Locate every Plasmodium falciparum-infected red blood cell.
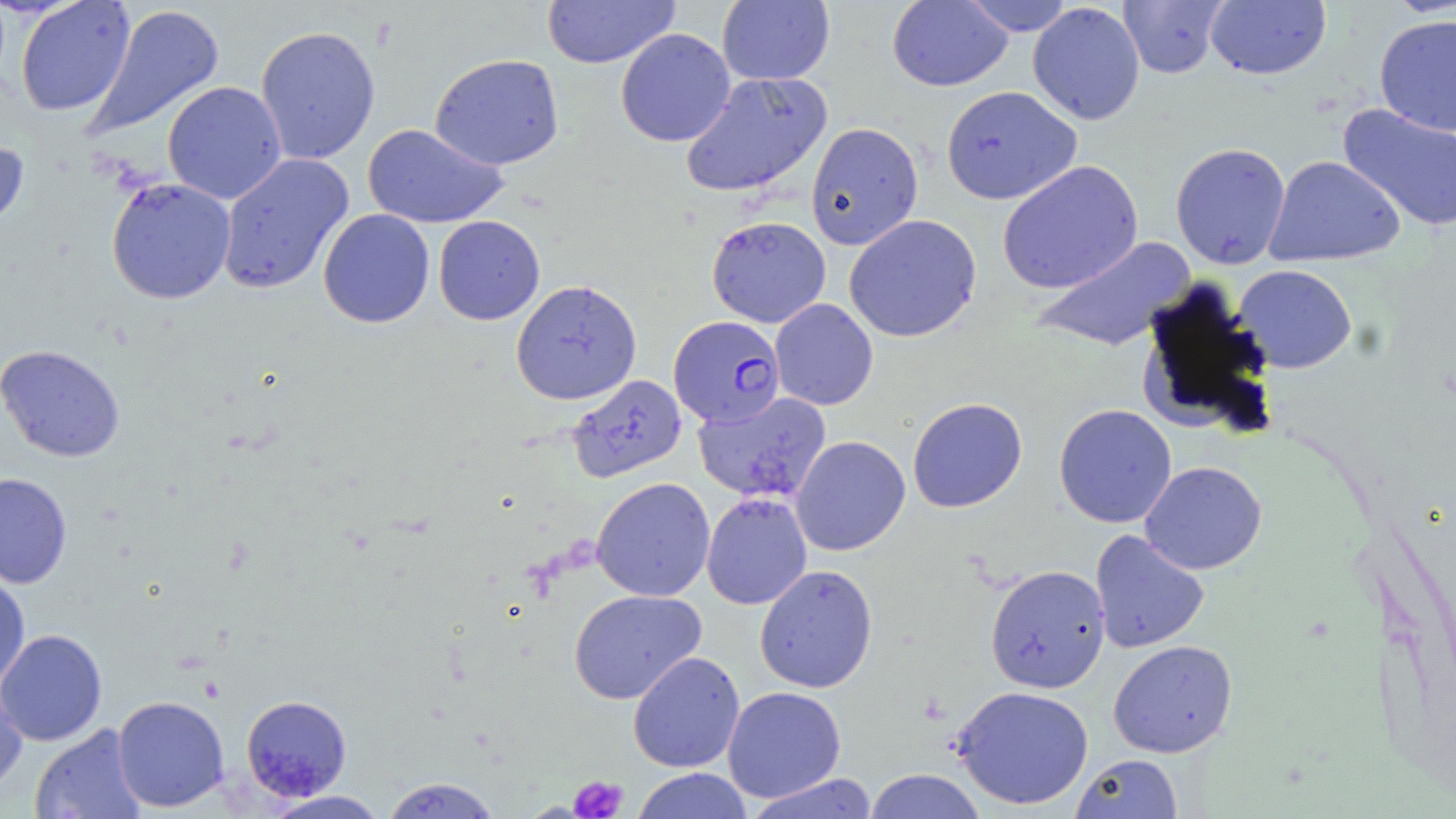
Approximate bounding boxes as (x1,y1)-(x2,y2) corner pairs in pixels.
Plasmodium falciparum-infected red blood cells: (668,315)-(786,427).

Uninfected red blood cell locations: (542,0)-(680,69), (887,0)-(1013,91), (960,0)-(1076,36), (1117,0)-(1228,79), (1205,0)-(1331,80), (15,1)-(136,117), (717,1)-(835,85), (1027,2)-(1145,126), (84,4)-(225,139), (1374,14)-(1456,137), (255,24)-(381,165), (615,28)-(736,147), (429,53)-(564,170), (679,70)-(833,198), (162,81)-(287,204), (941,85)-(1082,205), (1337,103)-(1456,233), (805,121)-(924,251), (362,123)-(508,229), (0,136)-(29,240), (1170,142)-(1291,269), (216,153)-(354,295), (1264,155)-(1406,267), (997,160)-(1143,294), (106,177)-(236,304), (318,209)-(435,328), (844,214)-(982,343), (433,215)-(545,325), (706,215)-(831,328), (1030,235)-(1197,352), (1232,264)-(1357,374), (1137,278)-(1278,440), (511,279)-(642,406), (769,299)-(878,410), (0,344)-(125,462), (567,374)-(687,483), (692,391)-(833,505), (907,397)-(1028,513), (1053,404)-(1177,528), (790,435)-(911,556), (1139,461)-(1267,575), (0,472)-(73,589), (591,477)-(715,601), (701,492)-(813,610), (1089,529)-(1210,654), (754,564)-(878,693), (985,564)-(1111,693), (0,571)-(30,692), (568,589)-(707,705), (0,628)-(107,746), (1108,640)-(1238,758), (628,651)-(745,773), (0,674)-(28,797), (951,684)-(1094,810), (722,686)-(846,802), (112,695)-(230,812), (240,695)-(352,800), (30,724)-(147,819), (1070,753)-(1183,819), (631,767)-(753,819), (863,768)-(987,818), (745,773)-(879,819), (380,777)-(503,818), (262,790)-(390,819). Platelet locations: (569,776)-(628,818). Slide-level diagnosis: Plasmodium falciparum. May-Grünwald-Giemsa-stained preparation. Optical microscopy. Thin blood film. Image is 1456×819 pixels. Captured at 1000x magnification. One field of a larger specimen.